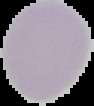
preparation = thin blood film
image size = 94×106 pixels
image type = segmented cell region with the area outside set to black
malaria status = uninfected